Name the parasite shown.
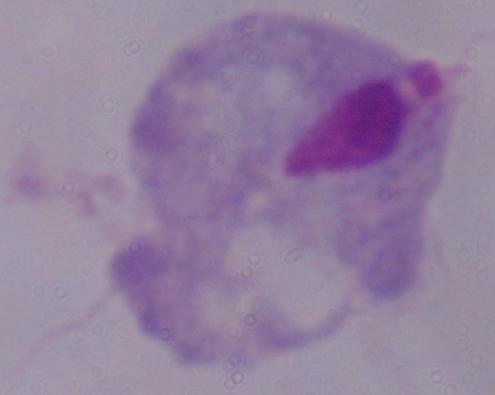
A trichomonad.

Summary:
  - Modality: photomicrograph
  - Magnification: 1000x